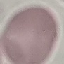

Summary:
  - Result: no malaria parasites seen
  - Image type: automatically extracted cell patch, resized to 64 × 64 pixels
  - Preparation: thin blood smear
  - Stain: Giemsa
  - Capture: smartphone camera at the microscope eyepiece